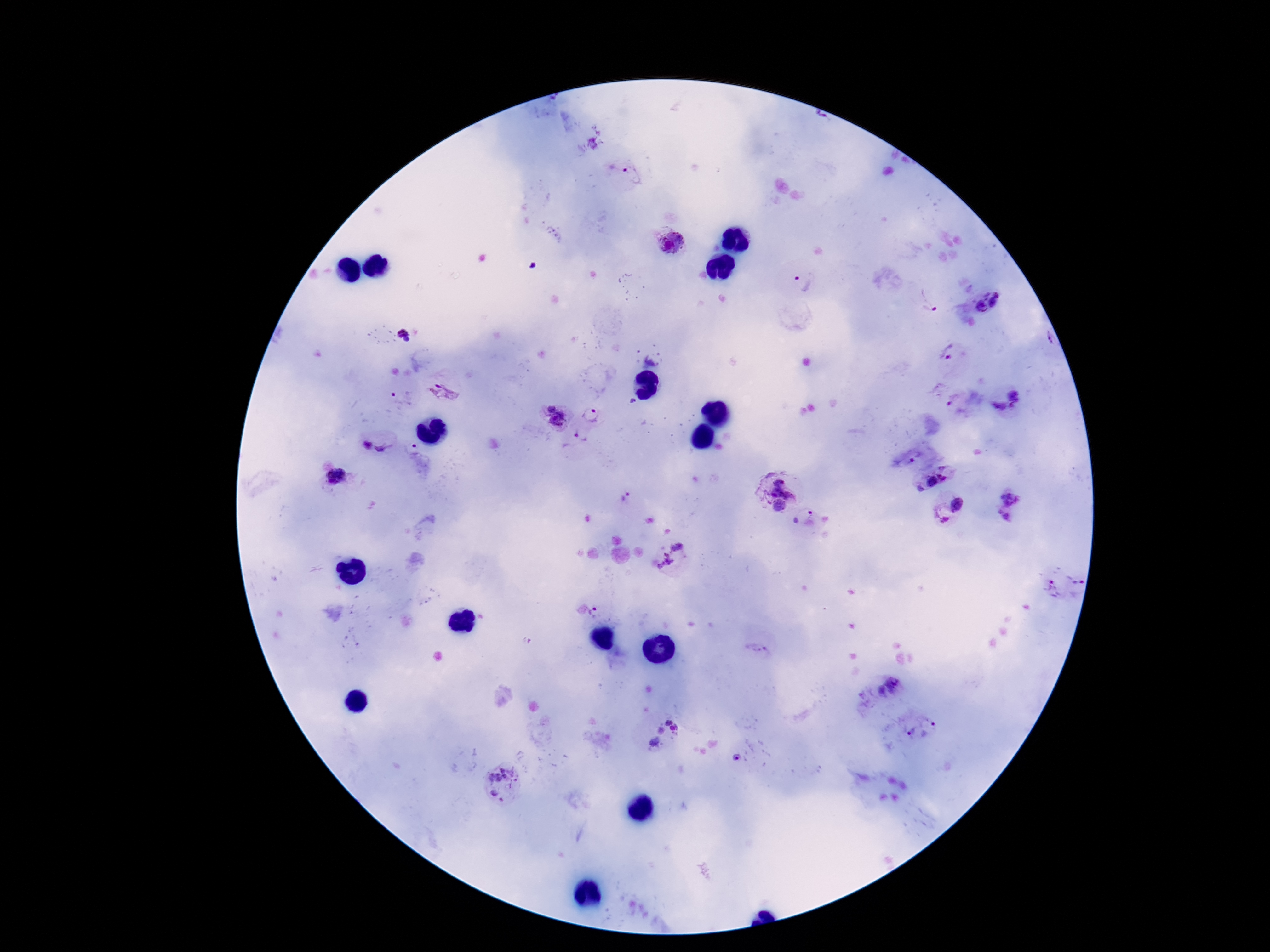
Approximate centers as (x, y) in pixels. Plasmodium parasite locations: (619, 169), (671, 242), (804, 281), (927, 301), (997, 301), (981, 305), (402, 329), (407, 340), (950, 353), (446, 387), (1014, 394), (402, 399), (550, 406), (1000, 408), (593, 415), (558, 419), (580, 437), (367, 446), (384, 448), (413, 448), (912, 461), (943, 467), (336, 476), (943, 478), (930, 481), (788, 483), (919, 490), (1011, 496), (626, 498), (958, 504), (779, 506), (810, 513), (941, 517), (1003, 517), (678, 547), (666, 561), (1076, 578), (1050, 589), (595, 608), (754, 648), (896, 682), (880, 691), (668, 722), (931, 724), (676, 729), (661, 730), (909, 732), (655, 743), (736, 758), (495, 770), (520, 777), (494, 793). Giemsa-stained preparation. Patient malaria status: positive. Image is 1270×952 pixels. Photographed through the microscope eyepiece with a smartphone camera. Thick blood film. 100x magnification. Single field of view.